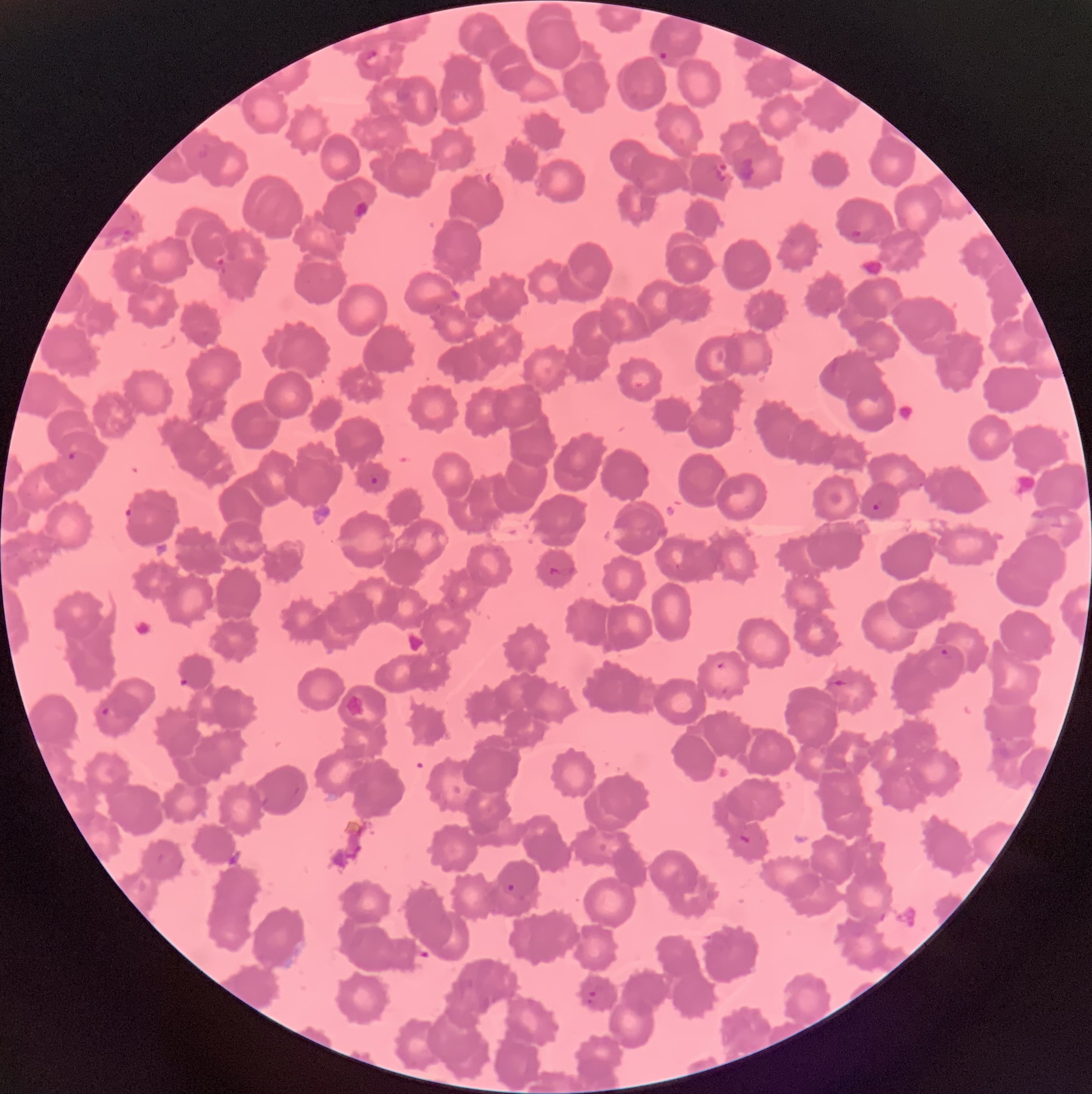

{
  "plasmodium_parasite_locations": "approximate bounding boxes as (x1,y1)-(x2,y2) corner pairs in pixels: (363,48)-(379,68), (657,50)-(670,62), (714,160)-(733,181), (849,228)-(865,240), (215,255)-(226,268), (67,450)-(77,461), (370,476)-(379,485), (870,502)-(881,513), (123,507)-(136,520), (938,646)-(950,658), (715,661)-(728,671), (832,674)-(851,689), (101,706)-(111,717), (738,832)-(751,846), (507,883)-(515,892), (586,990)-(597,1007)",
  "image_size": "1092×1094 pixels",
  "modality": "light microscopy",
  "preparation": "thin blood film",
  "red_blood_cell_morphology": "rouleaux formation"
}